Name the parasite shown.
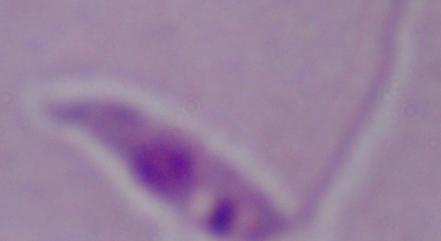
This is Leishmania.

1000x magnification. Micrograph.